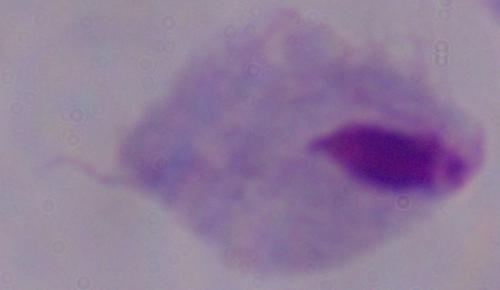

Summary:
  - Magnification: 1000x
  - Identification: trichomonad
  - Modality: micrograph